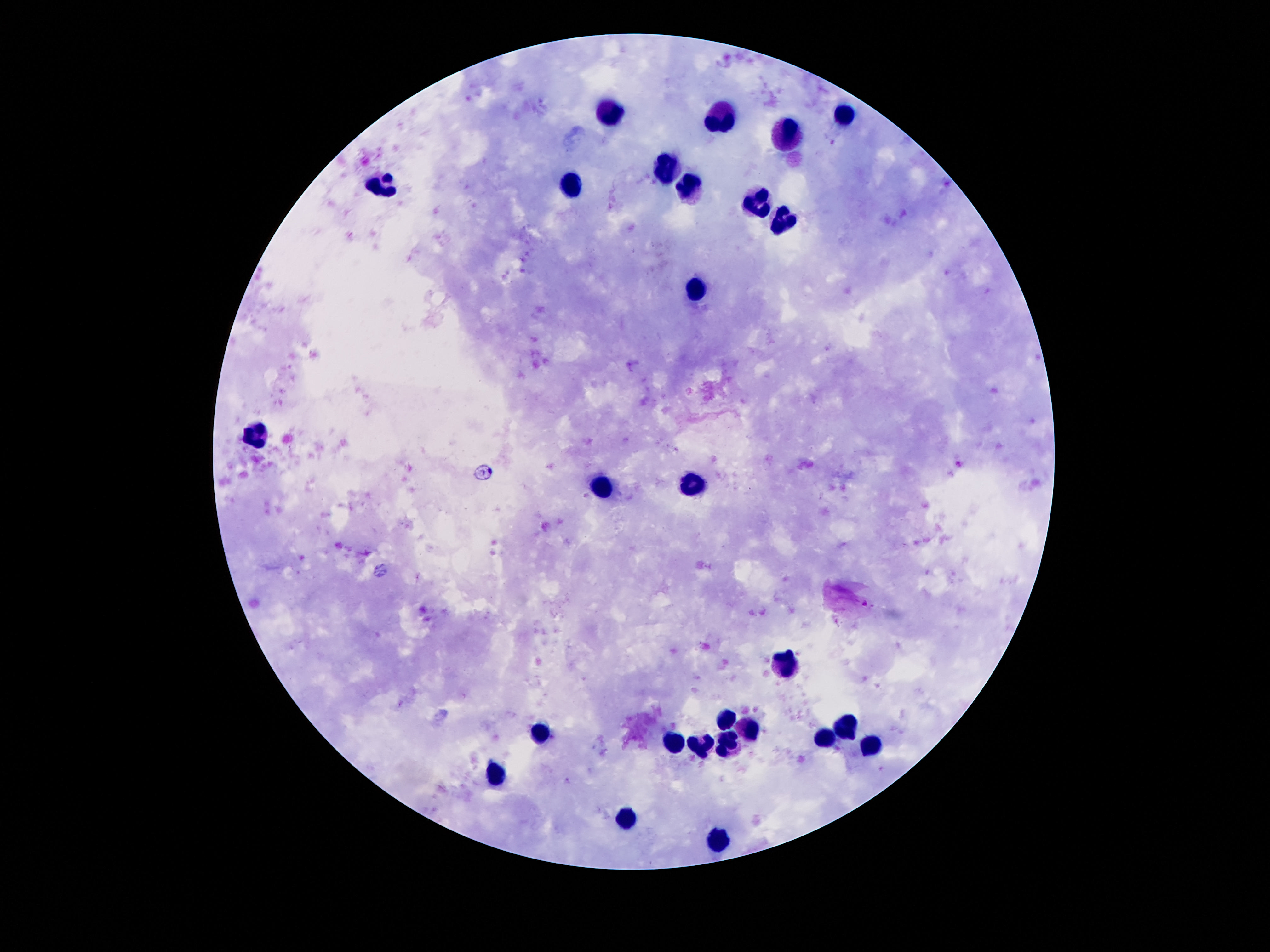
{
  "field_of_view": "single",
  "image_size": "1270×952 pixels",
  "stain": "Giemsa",
  "patient_malaria_status": "negative",
  "capture": "smartphone camera through the microscope eyepiece",
  "preparation": "thick blood film",
  "leukocyte_locations": "approximate centers as {x, y} in pixels: {611, 111}, {845, 113}, {723, 118}, {788, 134}, {669, 166}, {384, 186}, {570, 186}, {692, 188}, {758, 200}, {784, 222}, {697, 291}, {255, 436}, {690, 487}, {601, 489}, {784, 666}, {727, 721}, {750, 727}, {849, 727}, {539, 732}, {822, 739}, {674, 744}, {730, 744}, {702, 747}, {872, 747}, {498, 776}, {626, 818}, {720, 840}",
  "magnification": "100x"
}